Identify the parasite.
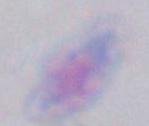
Toxoplasma gondii.

Micrograph. 1000x magnification.